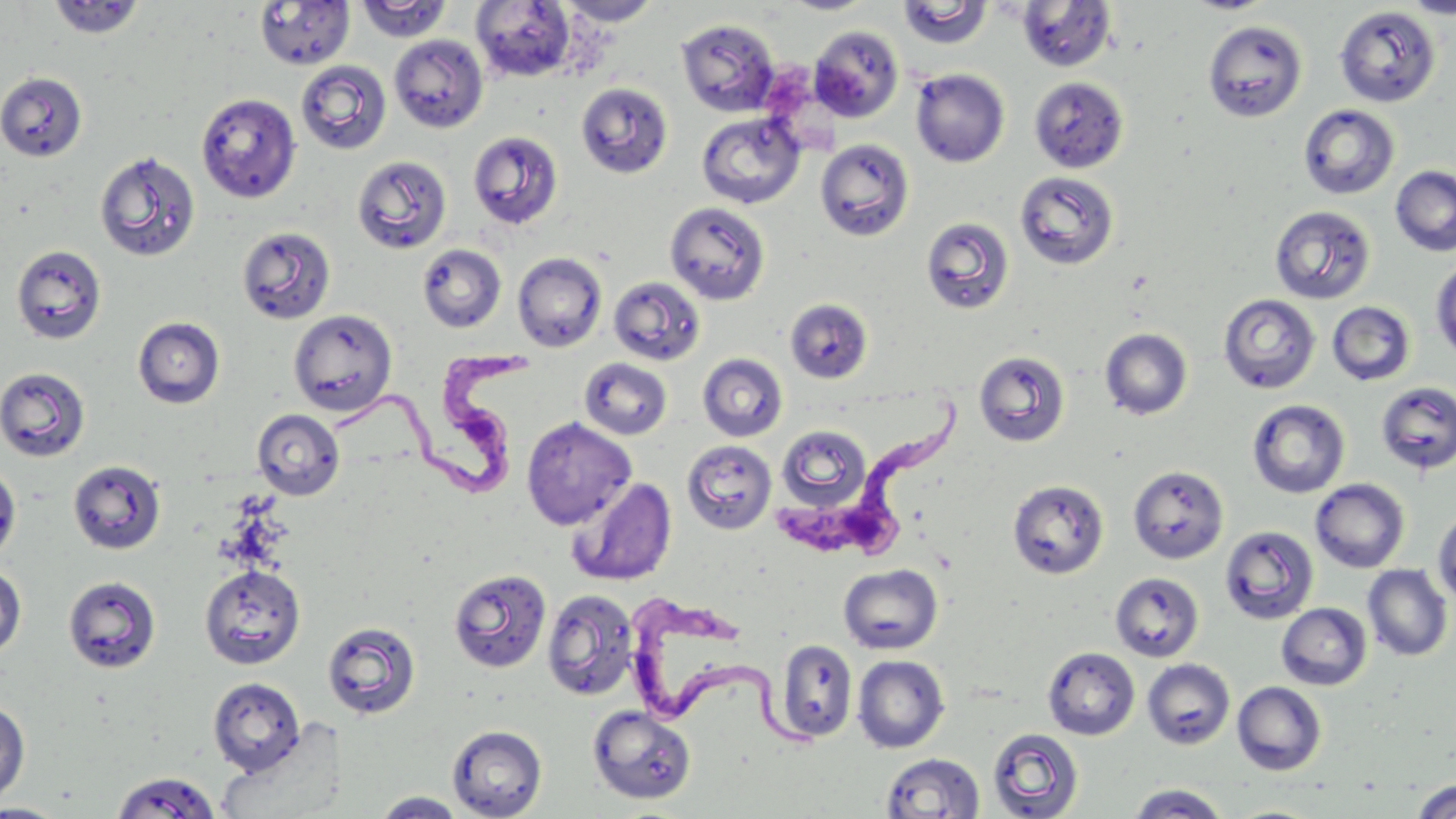

Approximate bounding boxes as named x1/y1/x2/y2 corners in pixels. Uninfected red blood cell locations: (x1=355, y1=0, x2=453, y2=43), (x1=782, y1=0, x2=875, y2=15), (x1=1185, y1=0, x2=1275, y2=14), (x1=1400, y1=0, x2=1456, y2=19), (x1=46, y1=1, x2=148, y2=40), (x1=254, y1=1, x2=355, y2=71), (x1=471, y1=1, x2=576, y2=82), (x1=556, y1=1, x2=662, y2=26), (x1=897, y1=1, x2=994, y2=49), (x1=1016, y1=1, x2=1117, y2=72), (x1=1334, y1=5, x2=1441, y2=108), (x1=677, y1=18, x2=781, y2=116), (x1=1203, y1=20, x2=1308, y2=123), (x1=808, y1=24, x2=904, y2=122), (x1=389, y1=35, x2=488, y2=133), (x1=296, y1=60, x2=392, y2=154), (x1=911, y1=68, x2=1010, y2=167), (x1=0, y1=72, x2=87, y2=162), (x1=1029, y1=76, x2=1129, y2=174), (x1=576, y1=82, x2=673, y2=178), (x1=196, y1=92, x2=302, y2=203), (x1=1298, y1=104, x2=1400, y2=200), (x1=696, y1=111, x2=806, y2=209), (x1=468, y1=130, x2=563, y2=230), (x1=814, y1=138, x2=915, y2=241), (x1=94, y1=150, x2=201, y2=262), (x1=352, y1=155, x2=452, y2=254), (x1=1390, y1=165, x2=1456, y2=257), (x1=1014, y1=171, x2=1119, y2=270), (x1=665, y1=202, x2=770, y2=305), (x1=1269, y1=205, x2=1376, y2=305), (x1=921, y1=217, x2=1015, y2=315), (x1=236, y1=226, x2=337, y2=325), (x1=11, y1=244, x2=107, y2=344), (x1=417, y1=244, x2=506, y2=333), (x1=512, y1=252, x2=608, y2=352), (x1=1431, y1=258, x2=1456, y2=362), (x1=608, y1=276, x2=706, y2=366), (x1=1218, y1=293, x2=1321, y2=395), (x1=785, y1=298, x2=873, y2=383), (x1=1326, y1=301, x2=1416, y2=386), (x1=288, y1=310, x2=398, y2=416), (x1=132, y1=316, x2=225, y2=409), (x1=1099, y1=327, x2=1193, y2=420), (x1=973, y1=350, x2=1071, y2=447), (x1=697, y1=353, x2=788, y2=442), (x1=579, y1=357, x2=673, y2=440), (x1=0, y1=366, x2=91, y2=462), (x1=1376, y1=382, x2=1456, y2=474), (x1=1247, y1=399, x2=1350, y2=498), (x1=251, y1=409, x2=345, y2=500), (x1=521, y1=417, x2=636, y2=529), (x1=776, y1=424, x2=872, y2=512), (x1=682, y1=440, x2=777, y2=535), (x1=67, y1=459, x2=167, y2=555), (x1=0, y1=461, x2=21, y2=563), (x1=1128, y1=465, x2=1229, y2=565), (x1=567, y1=476, x2=677, y2=587), (x1=1310, y1=478, x2=1410, y2=573), (x1=1008, y1=479, x2=1110, y2=579), (x1=1432, y1=506, x2=1456, y2=607), (x1=1219, y1=525, x2=1319, y2=625), (x1=838, y1=563, x2=943, y2=655), (x1=0, y1=564, x2=27, y2=660), (x1=199, y1=564, x2=306, y2=670), (x1=1363, y1=565, x2=1452, y2=662), (x1=448, y1=568, x2=552, y2=674), (x1=1110, y1=572, x2=1205, y2=662), (x1=62, y1=575, x2=162, y2=673), (x1=542, y1=588, x2=639, y2=701), (x1=1277, y1=602, x2=1372, y2=690), (x1=322, y1=619, x2=422, y2=720), (x1=773, y1=639, x2=858, y2=743), (x1=1043, y1=647, x2=1140, y2=740), (x1=852, y1=655, x2=950, y2=753), (x1=1142, y1=658, x2=1235, y2=749), (x1=208, y1=677, x2=305, y2=776), (x1=1233, y1=681, x2=1327, y2=775), (x1=0, y1=700, x2=30, y2=806), (x1=587, y1=705, x2=696, y2=804), (x1=447, y1=724, x2=547, y2=818), (x1=987, y1=728, x2=1084, y2=818), (x1=880, y1=752, x2=985, y2=818), (x1=111, y1=771, x2=221, y2=818), (x1=1412, y1=779, x2=1456, y2=819), (x1=1126, y1=784, x2=1230, y2=818), (x1=370, y1=791, x2=468, y2=818), (x1=1, y1=803, x2=69, y2=819). Trypanosoma brucei locations: (x1=339, y1=340, x2=548, y2=495), (x1=775, y1=397, x2=965, y2=564), (x1=622, y1=593, x2=823, y2=750). Slide-level diagnosis: Trypanosoma brucei. 1000x magnification. Optical microscopy. One field of a larger specimen. May-Grünwald-Giemsa-stained preparation. Thin blood film. Image is 1456×819 pixels.